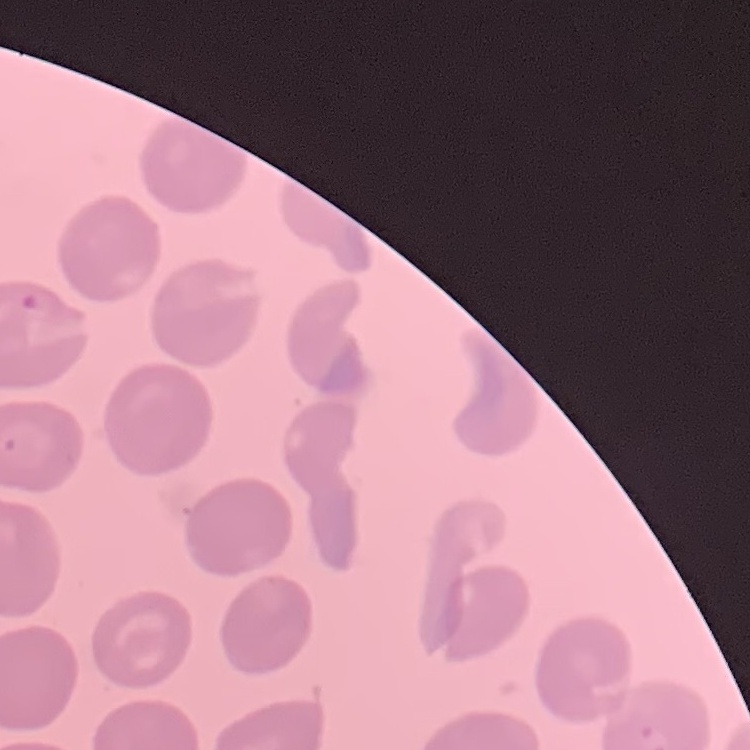
The red blood cells show no rouleaux formation. Stained with either Field's or Giemsa. One tile cut from a larger photomicrograph. Thin blood smear.